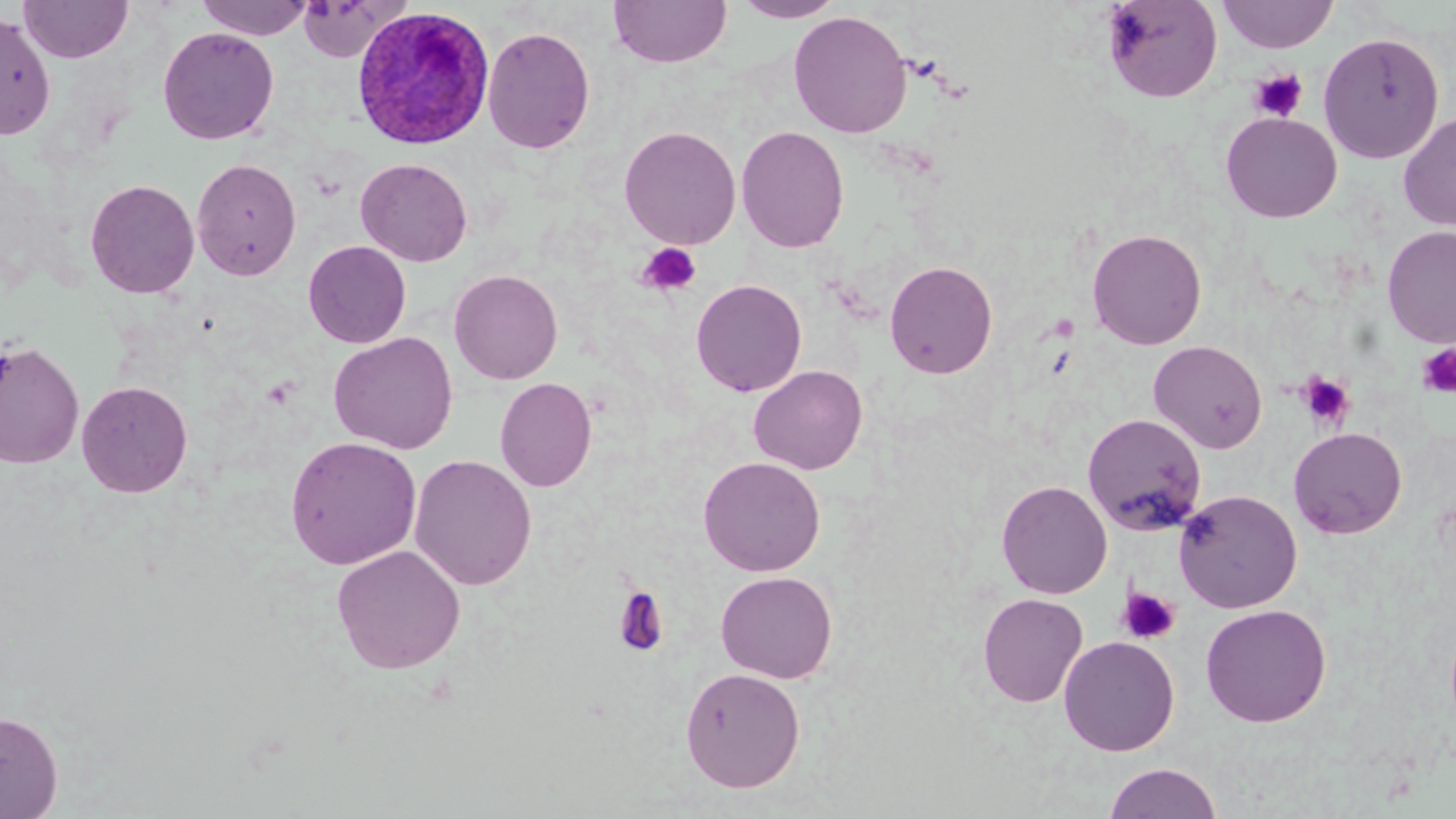
Summary:
  - Coordinate format: approximate bounding boxes as named x1/y1/x2/y2 corners in pixels
  - Uninfected red blood cell locations: (x1=195, y1=0, x2=315, y2=39), (x1=295, y1=0, x2=407, y2=62), (x1=608, y1=0, x2=732, y2=68), (x1=733, y1=0, x2=845, y2=22), (x1=1101, y1=0, x2=1222, y2=102), (x1=1217, y1=0, x2=1339, y2=53), (x1=18, y1=1, x2=133, y2=63), (x1=0, y1=10, x2=56, y2=141), (x1=788, y1=10, x2=912, y2=138), (x1=482, y1=25, x2=596, y2=155), (x1=157, y1=26, x2=280, y2=145), (x1=1318, y1=31, x2=1444, y2=164), (x1=1220, y1=111, x2=1342, y2=223), (x1=1398, y1=113, x2=1456, y2=232), (x1=619, y1=125, x2=741, y2=250), (x1=736, y1=125, x2=850, y2=253), (x1=191, y1=157, x2=302, y2=281), (x1=355, y1=157, x2=472, y2=266), (x1=84, y1=178, x2=200, y2=298), (x1=1382, y1=225, x2=1456, y2=348), (x1=1087, y1=227, x2=1207, y2=350), (x1=303, y1=240, x2=411, y2=348), (x1=884, y1=260, x2=998, y2=379), (x1=448, y1=269, x2=563, y2=385), (x1=691, y1=278, x2=807, y2=397), (x1=328, y1=331, x2=459, y2=454), (x1=1148, y1=339, x2=1268, y2=453), (x1=0, y1=340, x2=85, y2=469), (x1=748, y1=365, x2=868, y2=475), (x1=495, y1=377, x2=597, y2=492), (x1=76, y1=380, x2=194, y2=498), (x1=1082, y1=413, x2=1207, y2=535), (x1=1288, y1=427, x2=1407, y2=539), (x1=285, y1=436, x2=422, y2=570), (x1=409, y1=454, x2=537, y2=591), (x1=697, y1=456, x2=826, y2=576), (x1=996, y1=479, x2=1113, y2=598), (x1=1173, y1=489, x2=1303, y2=613), (x1=331, y1=544, x2=466, y2=674), (x1=715, y1=570, x2=838, y2=683), (x1=977, y1=593, x2=1088, y2=708), (x1=1200, y1=603, x2=1332, y2=727), (x1=1059, y1=635, x2=1180, y2=756), (x1=680, y1=666, x2=805, y2=792), (x1=0, y1=710, x2=63, y2=818), (x1=1103, y1=762, x2=1223, y2=818)
  - Platelet locations: (x1=1249, y1=68, x2=1307, y2=122), (x1=637, y1=243, x2=702, y2=297), (x1=1417, y1=344, x2=1456, y2=398), (x1=1298, y1=372, x2=1355, y2=429), (x1=612, y1=584, x2=669, y2=658), (x1=1116, y1=587, x2=1181, y2=645)
  - Plasmodium ovale-infected red blood cell locations: (x1=351, y1=6, x2=494, y2=149)
  - Slide-level diagnosis: Plasmodium ovale
  - Preparation: thin blood film
  - Image size: 1456×819 pixels
  - Modality: optical microscopy
  - Magnification: 1000x
  - Stain: May-Grünwald-Giemsa
  - Field of view: single